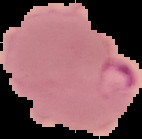

From a thin blood film. Image is 142×139 pixels. Cell region segmented out of the field of view; the surrounding area is masked to black. Malaria status: parasitized.